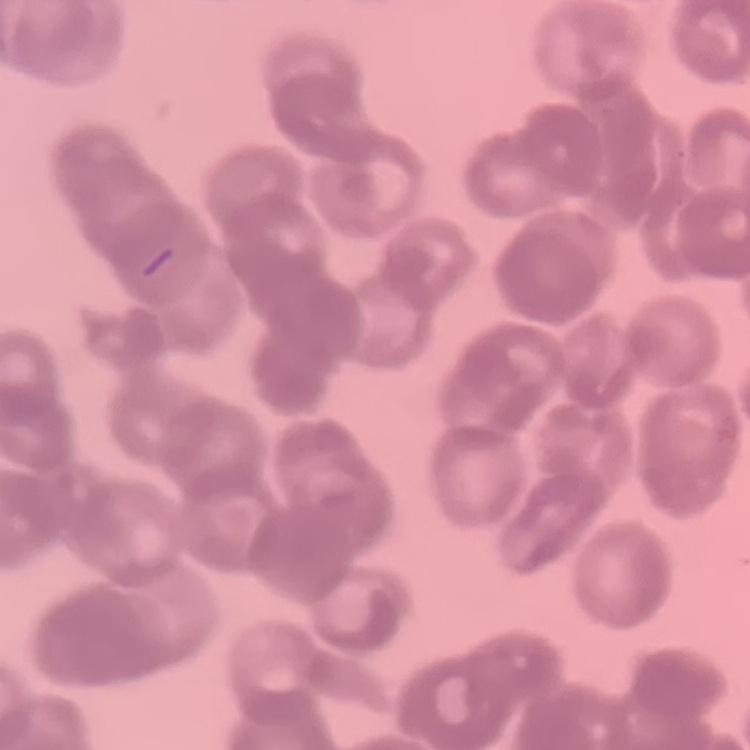
The red blood cells show rouleaux formation. One tile cut from a larger photomicrograph. Stained with either Field's or Giemsa. Thin peripheral smear.